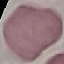

Malaria status: uninfected. Photographed with a smartphone camera at the microscope eyepiece. Thin blood film. Automatically extracted cell patch, resized to 64 × 64 pixels. Giemsa-stained preparation.